Identify the parasite.
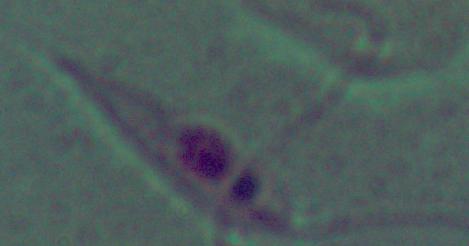

This is Leishmania.

1000x magnification. Micrograph.